Assess this cell for malaria.
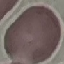

It is uninfected.

image type = cell patch, automatically extracted from a larger field of view and resized to 64 × 64 pixels
stain = Giemsa
preparation = thin blood smear
capture = smartphone camera at the microscope eyepiece